Identify the parasite.
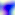
Toxoplasma gondii.

400x magnification. Photomicrograph.